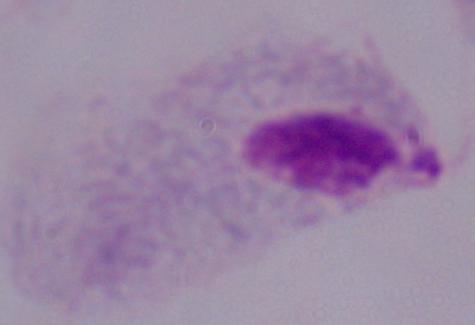 1000x magnification. A trichomonad is shown. Photomicrograph.